Locate every Plasmodium ovale-infected red blood cell.
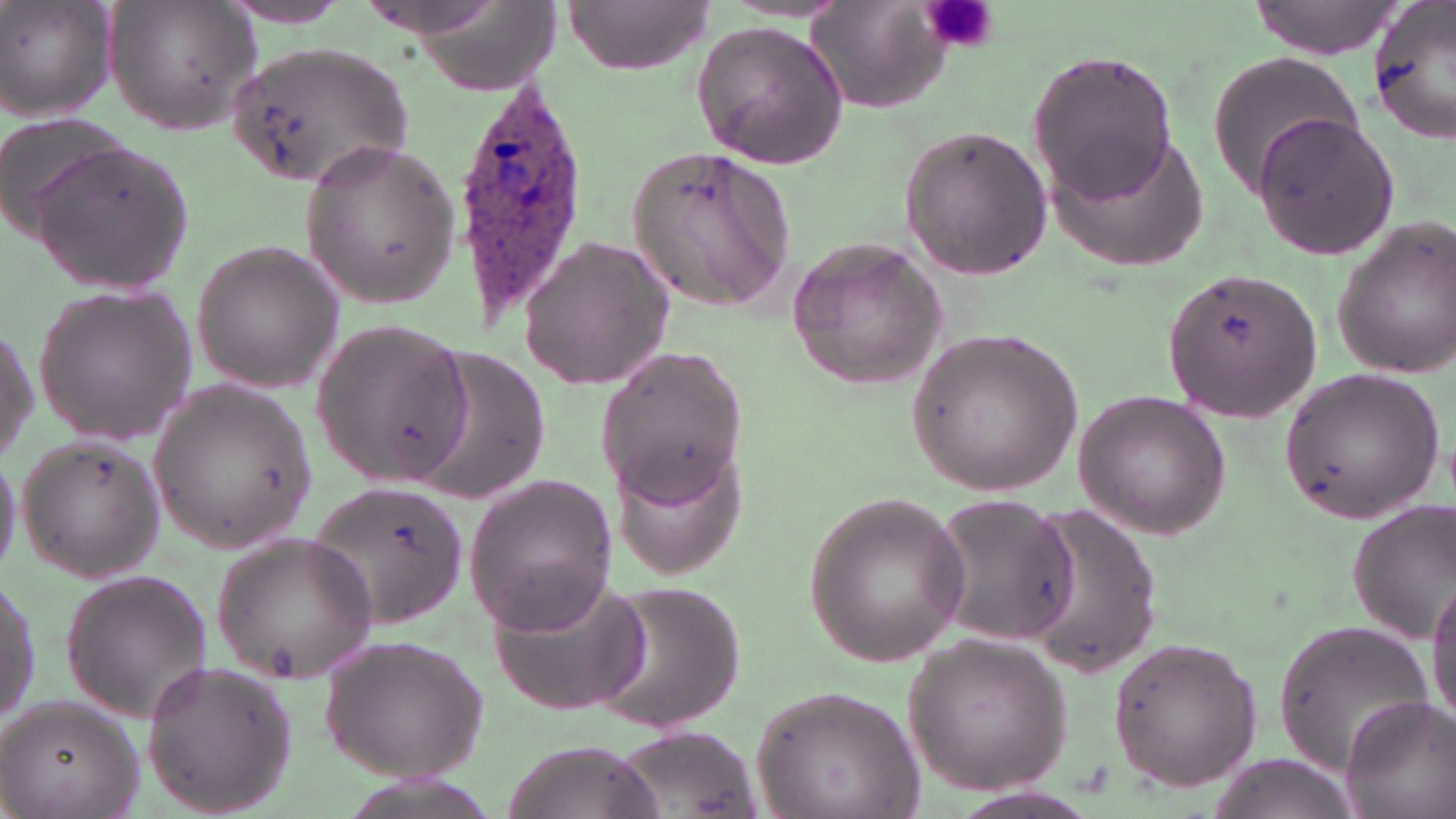

Approximate bounding boxes as (x1, y1, x2, y2) in pixels.
Plasmodium ovale-infected red blood cells: (449, 73, 591, 328).

{
  "slide_level_diagnosis": "Plasmodium ovale",
  "image_size": "1456×819 pixels",
  "platelet_locations": "approximate bounding boxes as (x1, y1, x2, y2) in pixels: (918, 0, 998, 55)",
  "uninfected_red_blood_cell_locations": "approximate bounding boxes as (x1, y1, x2, y2) in pixels: (807, 0, 957, 115), (1248, 0, 1402, 57), (565, 1, 713, 74), (1365, 1, 1456, 145), (103, 2, 260, 135), (0, 3, 118, 122), (216, 4, 361, 27), (689, 21, 851, 167), (229, 42, 411, 195), (1027, 48, 1180, 202), (1205, 53, 1366, 199), (0, 110, 128, 239), (1251, 112, 1401, 257), (895, 124, 1053, 281), (1040, 124, 1211, 279), (299, 136, 460, 308), (31, 139, 195, 300), (625, 145, 796, 315), (1329, 215, 1456, 378), (787, 232, 949, 394), (517, 235, 675, 391), (189, 237, 345, 393), (1159, 269, 1323, 421), (29, 281, 201, 446), (310, 316, 473, 486), (0, 319, 37, 470), (907, 325, 1082, 495), (594, 346, 747, 503), (413, 349, 553, 502), (1277, 367, 1445, 523), (150, 382, 314, 550), (1074, 389, 1231, 540), (610, 436, 748, 579), (17, 437, 167, 582), (0, 445, 24, 581), (463, 472, 621, 634), (307, 481, 470, 629), (800, 490, 970, 668), (925, 491, 1076, 649), (1345, 498, 1455, 643), (1009, 503, 1164, 673), (212, 531, 378, 683), (60, 569, 212, 723), (1, 570, 40, 733), (1428, 570, 1456, 729), (588, 575, 745, 731), (490, 578, 651, 715), (1274, 621, 1435, 775), (321, 633, 487, 783), (903, 635, 1072, 795), (1106, 635, 1263, 791), (139, 657, 299, 816), (749, 684, 923, 819), (0, 694, 146, 819), (1338, 695, 1456, 819), (610, 726, 761, 816), (499, 741, 667, 819), (1202, 756, 1364, 819)",
  "stain": "May-Grünwald-Giemsa",
  "preparation": "thin blood smear",
  "magnification": "1000x",
  "modality": "optical microscopy",
  "field_of_view": "one of a larger specimen"
}